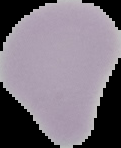
From a thin blood smear. Result: negative for Plasmodium parasites. Segmented cell region on a black background. Image is 121×148 pixels.